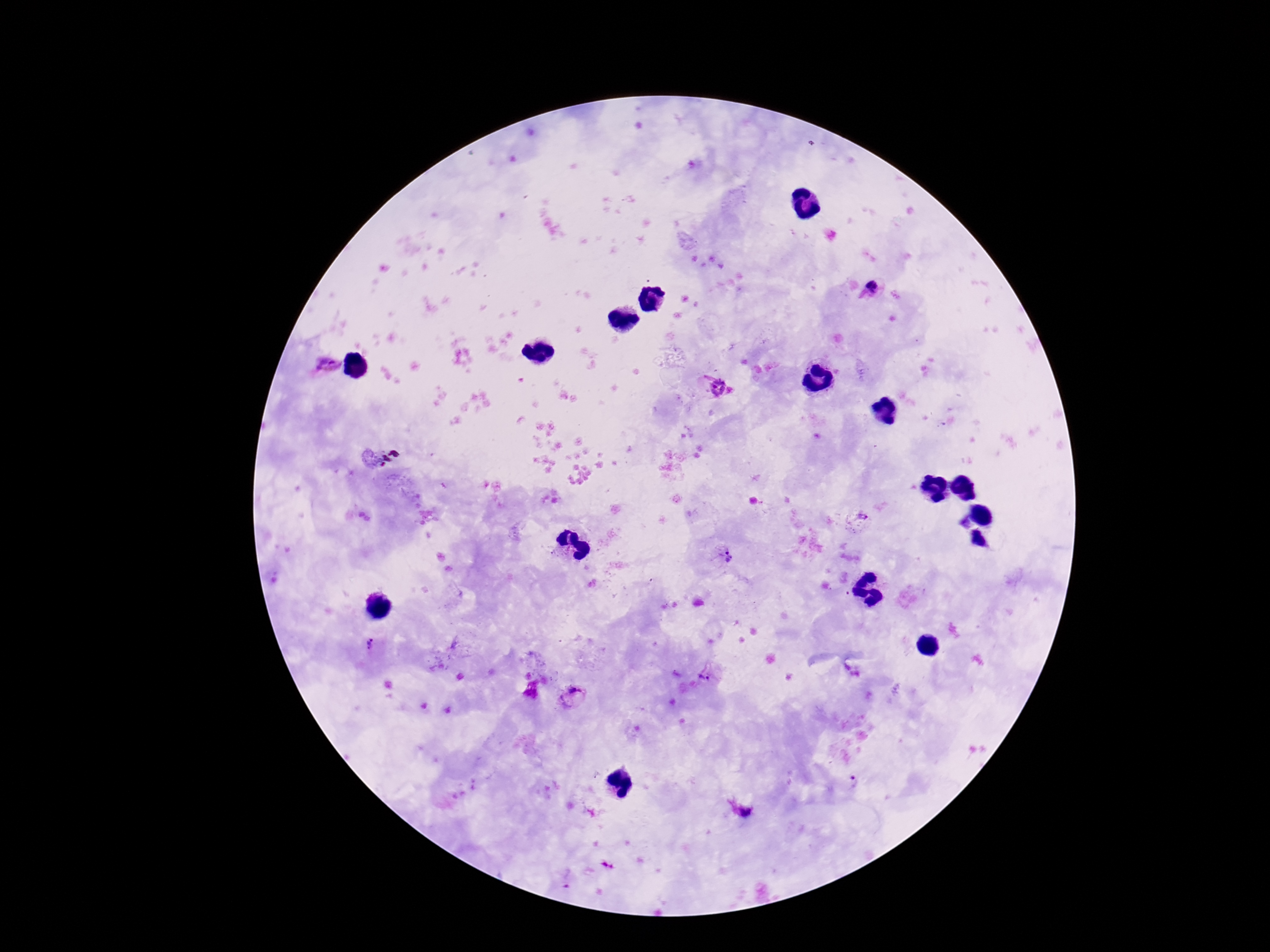 Approximate centers as {x, y} in pixels. Plasmodium parasite locations: {872, 286}, {326, 365}, {715, 386}, {861, 519}, {728, 552}, {729, 560}, {371, 643}, {528, 674}, {705, 677}, {534, 682}, {530, 694}, {571, 698}, {746, 813}, {607, 865}. Image is 1270×952 pixels. Patient malaria status: positive. Thick blood smear. Photographed through the microscope eyepiece with a smartphone camera. 100x magnification. Single field of view. Giemsa stain.